Name the parasite shown.
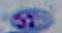

This is Toxoplasma gondii.

Summary:
  - Magnification: 1000x
  - Modality: micrograph